State the blood parasite species.
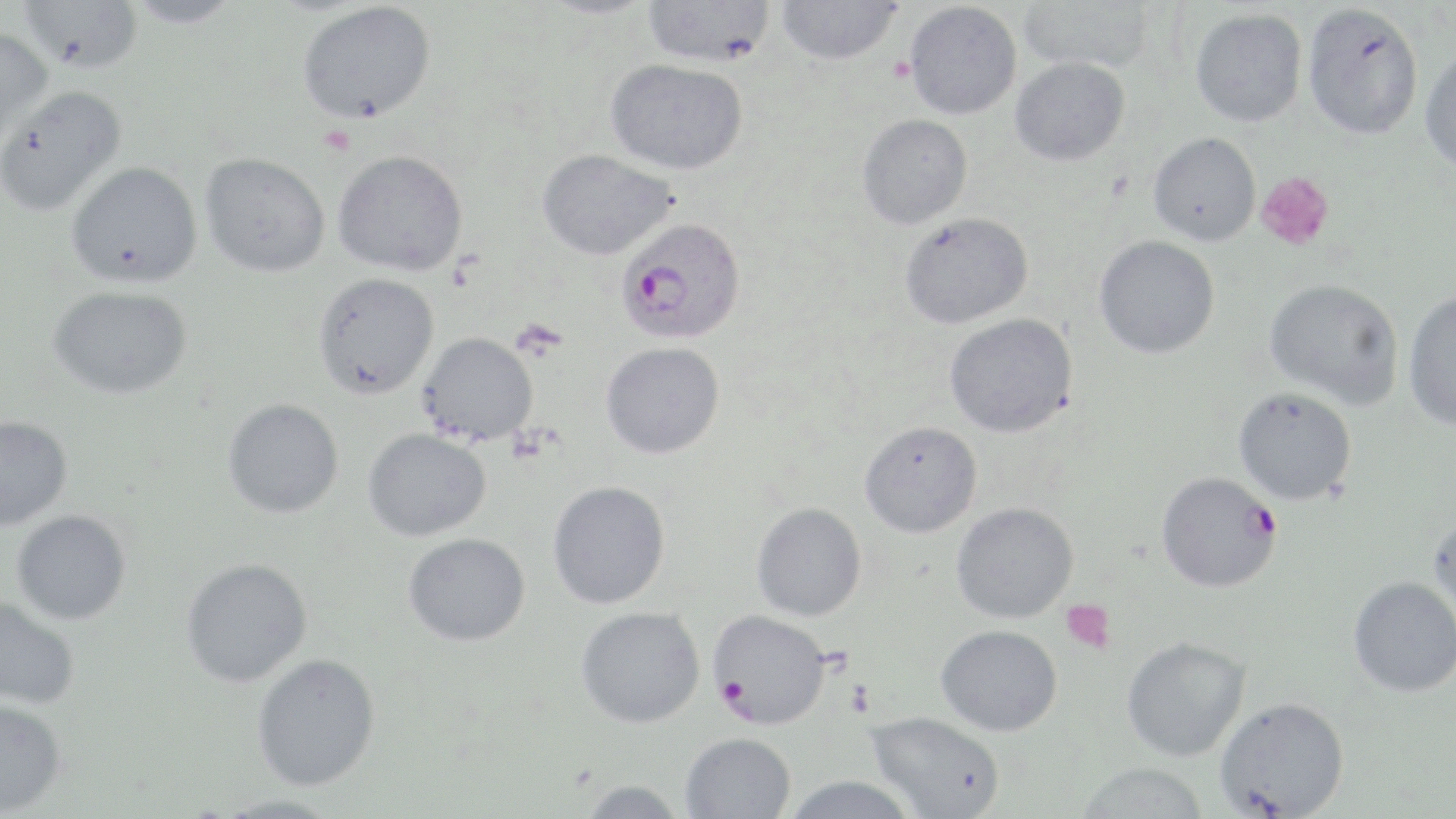
Plasmodium falciparum.

Summary:
  - Coordinate format: approximate bounding boxes as named x1/y1/x2/y2 corners in pixels
  - Plasmodium falciparum-infected red blood cell locations: (x1=618, y1=224, x2=749, y2=342), (x1=1156, y1=471, x2=1281, y2=593), (x1=708, y1=609, x2=832, y2=729)
  - Platelet locations: (x1=1256, y1=172, x2=1334, y2=251), (x1=1060, y1=599, x2=1115, y2=653)
  - Uninfected red blood cell locations: (x1=18, y1=0, x2=143, y2=74), (x1=125, y1=0, x2=242, y2=28), (x1=533, y1=0, x2=660, y2=19), (x1=643, y1=0, x2=776, y2=67), (x1=1018, y1=0, x2=1154, y2=73), (x1=776, y1=1, x2=902, y2=65), (x1=297, y1=2, x2=436, y2=124), (x1=904, y1=2, x2=1022, y2=119), (x1=1302, y1=3, x2=1423, y2=139), (x1=1189, y1=8, x2=1307, y2=126), (x1=0, y1=25, x2=53, y2=147), (x1=1419, y1=47, x2=1456, y2=173), (x1=1009, y1=57, x2=1130, y2=166), (x1=605, y1=58, x2=748, y2=175), (x1=0, y1=84, x2=129, y2=218), (x1=857, y1=113, x2=973, y2=229), (x1=1148, y1=132, x2=1261, y2=245), (x1=332, y1=149, x2=468, y2=276), (x1=537, y1=149, x2=678, y2=260), (x1=200, y1=152, x2=330, y2=277), (x1=65, y1=161, x2=203, y2=288), (x1=899, y1=212, x2=1033, y2=329), (x1=1094, y1=235, x2=1220, y2=358), (x1=312, y1=272, x2=439, y2=400), (x1=1264, y1=279, x2=1403, y2=408), (x1=47, y1=285, x2=194, y2=399), (x1=1403, y1=289, x2=1456, y2=431), (x1=944, y1=313, x2=1079, y2=438), (x1=418, y1=332, x2=538, y2=445), (x1=600, y1=341, x2=724, y2=459), (x1=1233, y1=387, x2=1357, y2=505), (x1=222, y1=398, x2=344, y2=518), (x1=0, y1=415, x2=73, y2=531), (x1=859, y1=421, x2=983, y2=538), (x1=362, y1=428, x2=491, y2=541), (x1=547, y1=480, x2=670, y2=609), (x1=951, y1=501, x2=1078, y2=624), (x1=751, y1=502, x2=867, y2=621), (x1=11, y1=509, x2=132, y2=625), (x1=1427, y1=512, x2=1456, y2=631), (x1=403, y1=532, x2=531, y2=646), (x1=180, y1=558, x2=314, y2=687), (x1=1347, y1=576, x2=1456, y2=697), (x1=0, y1=596, x2=81, y2=710), (x1=576, y1=606, x2=705, y2=728), (x1=935, y1=624, x2=1062, y2=736), (x1=1120, y1=636, x2=1251, y2=762), (x1=251, y1=653, x2=381, y2=791), (x1=1214, y1=696, x2=1350, y2=818), (x1=0, y1=698, x2=67, y2=816), (x1=866, y1=711, x2=1005, y2=818), (x1=680, y1=732, x2=796, y2=819), (x1=1075, y1=762, x2=1209, y2=819), (x1=781, y1=775, x2=923, y2=819), (x1=580, y1=778, x2=686, y2=818), (x1=210, y1=794, x2=344, y2=819)
  - Image size: 1456×819 pixels
  - Modality: optical microscopy
  - Magnification: 1000x
  - Field of view: single
  - Stain: May-Grünwald-Giemsa
  - Preparation: thin blood film